Locate and identify every blood parasite.
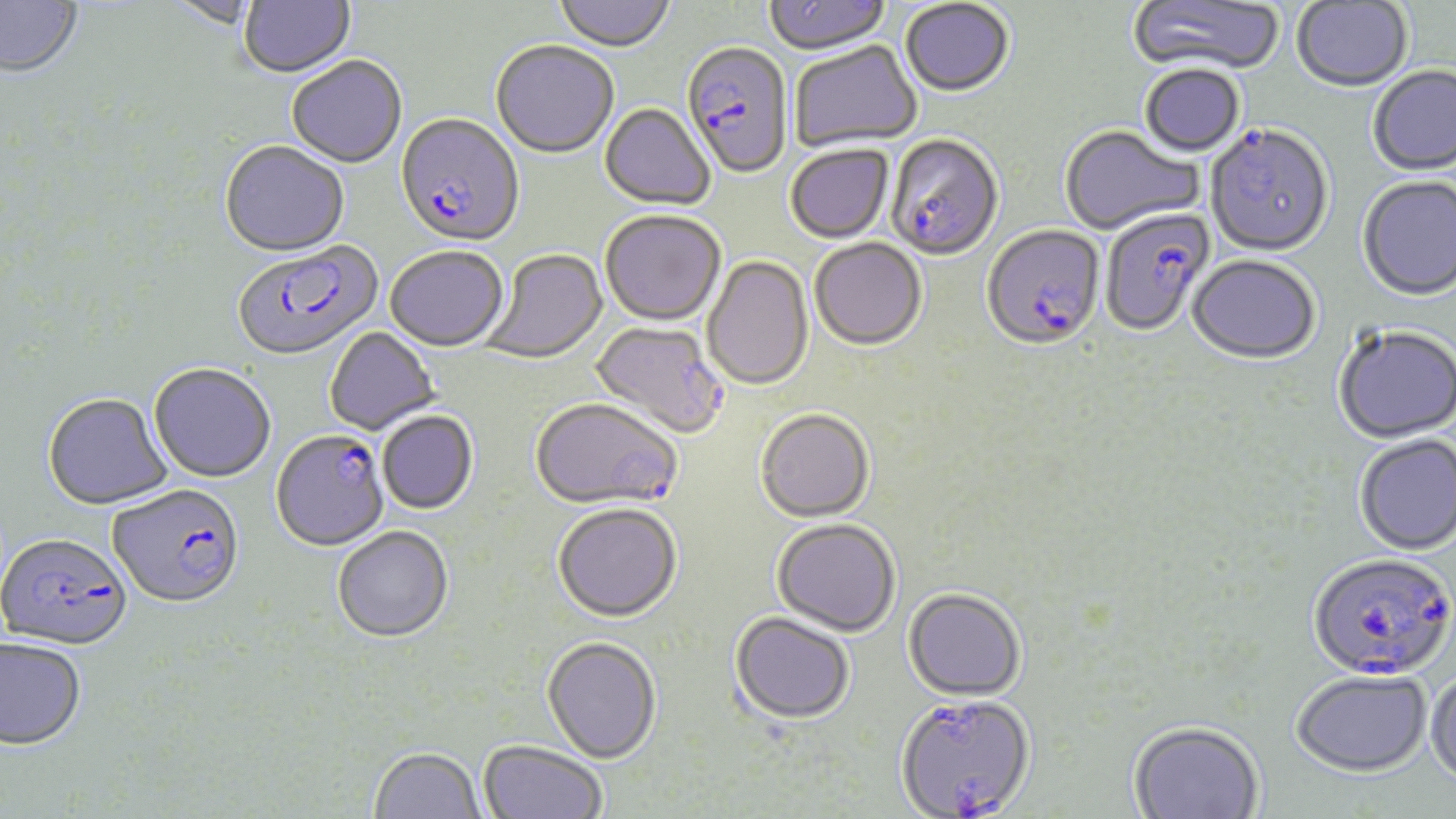

Approximate bounding boxes as (x1, y1, x2, y2) in pixels.
Plasmodium falciparum-infected red blood cells: (681, 45, 793, 180), (395, 116, 524, 250), (1205, 127, 1334, 260), (885, 137, 1004, 263), (1100, 209, 1214, 337), (981, 227, 1105, 354), (232, 244, 383, 363), (589, 321, 728, 443), (530, 399, 681, 512), (271, 431, 389, 553), (108, 487, 244, 612), (1, 535, 132, 654), (1307, 554, 1454, 684), (895, 695, 1035, 819).
No Plasmodium ovale, Plasmodium malariae, Plasmodium vivax, Babesia divergens, or Trypanosoma brucei observed.

Summary:
  - Uninfected red blood cell locations: (239, 0, 356, 81), (554, 0, 675, 55), (765, 0, 892, 58), (1127, 0, 1285, 77), (0, 1, 82, 79), (161, 1, 261, 31), (900, 1, 1014, 99), (1291, 1, 1413, 94), (790, 42, 922, 152), (491, 43, 618, 160), (287, 58, 407, 170), (1140, 66, 1244, 159), (1368, 68, 1456, 177), (599, 104, 715, 212), (1059, 126, 1204, 236), (220, 143, 350, 260), (786, 146, 893, 245), (1357, 177, 1456, 304), (600, 212, 726, 328), (810, 240, 927, 353), (385, 248, 508, 353), (481, 250, 609, 365), (702, 256, 814, 393), (1187, 257, 1320, 367), (1333, 327, 1456, 445), (325, 328, 441, 436), (149, 365, 276, 485), (42, 394, 174, 513), (755, 411, 875, 525), (377, 412, 479, 516), (1354, 435, 1456, 557), (553, 506, 682, 625), (771, 521, 900, 639), (333, 528, 454, 645), (903, 590, 1026, 703), (729, 615, 854, 728), (542, 639, 661, 765), (0, 640, 86, 751), (1426, 666, 1456, 789), (1292, 672, 1432, 778), (1129, 722, 1263, 818), (477, 742, 607, 819), (370, 749, 485, 819)
  - Slide-level diagnosis: Plasmodium falciparum
  - Stain: May-Grünwald-Giemsa
  - Magnification: 1000x
  - Modality: light microscopy
  - Field of view: one of a larger specimen
  - Image size: 1456×819 pixels
  - Preparation: thin blood smear